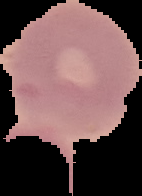
malaria status = uninfected
image type = cell region segmented out of the field of view; surrounding area masked to black
image size = 142×196 pixels
preparation = thin blood film